Classify this cell by malaria status.
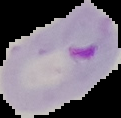
Parasitized.

Summary:
  - Image size: 121×118 pixels
  - Image type: cell region segmented out of the field of view; surrounding area masked to black
  - Preparation: thin blood film